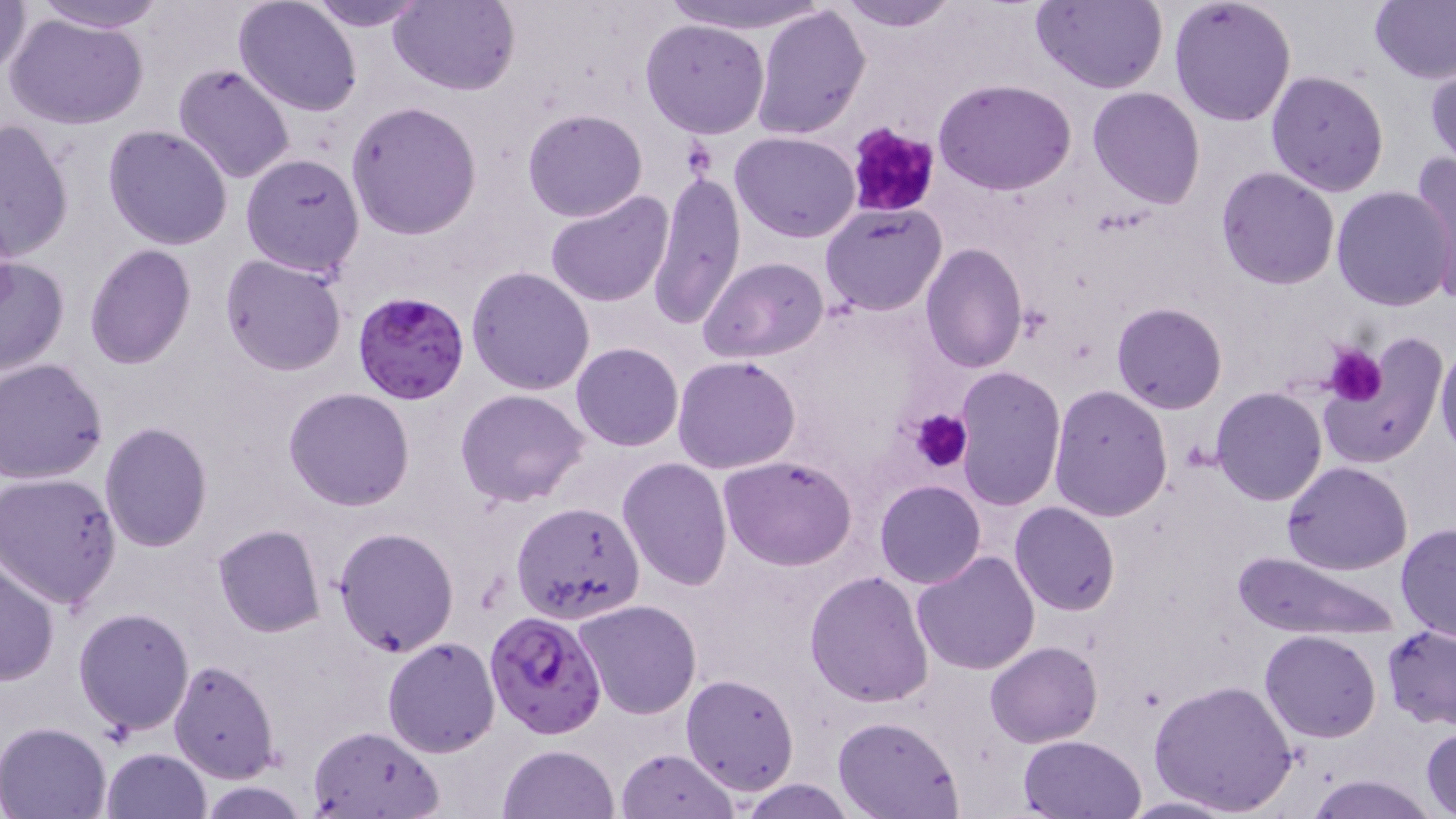
Plasmodium falciparum-infected red blood cell locations = approximate bounding boxes as (x1, y1, x2, y2) in pixels: (353, 291, 468, 405), (483, 608, 608, 740)
slide-level diagnosis = Plasmodium falciparum
uninfected red blood cell locations = approximate bounding boxes as (x1, y1, x2, y2) in pixels: (0, 0, 34, 82), (28, 0, 169, 33), (306, 0, 432, 30), (390, 0, 517, 96), (663, 0, 836, 36), (834, 0, 963, 31), (1030, 0, 1168, 92), (1168, 0, 1297, 126), (1368, 0, 1456, 84), (235, 1, 363, 117), (751, 4, 871, 139), (5, 12, 149, 131), (640, 18, 770, 138), (172, 63, 297, 185), (1426, 66, 1456, 168), (1266, 69, 1390, 197), (934, 78, 1077, 195), (1087, 85, 1207, 210), (346, 100, 482, 239), (521, 108, 649, 222), (0, 119, 72, 262), (103, 124, 233, 250), (731, 131, 860, 241), (1411, 151, 1456, 298), (240, 154, 365, 279), (1215, 165, 1341, 289), (646, 172, 747, 329), (1331, 186, 1454, 312), (544, 190, 675, 310), (819, 203, 948, 316), (920, 243, 1026, 371), (83, 244, 196, 369), (220, 253, 348, 375), (0, 255, 70, 379), (699, 257, 830, 364), (467, 265, 597, 394), (1111, 302, 1226, 414), (1322, 330, 1445, 468), (1435, 338, 1456, 464), (571, 343, 683, 451), (673, 356, 801, 474), (1, 358, 109, 484), (953, 364, 1066, 511), (1048, 384, 1174, 522), (1209, 387, 1328, 507), (283, 388, 414, 511), (456, 388, 588, 508), (99, 422, 212, 552), (720, 456, 857, 570), (617, 457, 734, 591), (1280, 462, 1414, 576), (0, 474, 122, 608), (875, 479, 986, 588), (1009, 502, 1120, 617), (511, 503, 642, 627), (1396, 522, 1455, 643), (213, 525, 325, 638), (333, 526, 459, 657), (1234, 550, 1399, 641), (911, 551, 1041, 676), (0, 557, 59, 687), (804, 570, 933, 707), (574, 600, 703, 720), (73, 607, 195, 737), (1382, 625, 1456, 729), (1260, 630, 1382, 743), (382, 636, 501, 757), (985, 641, 1102, 748), (168, 660, 278, 782), (680, 673, 799, 795), (1150, 677, 1297, 817), (832, 715, 963, 818), (0, 722, 114, 818), (306, 726, 445, 819), (1421, 728, 1455, 817), (1018, 735, 1147, 819), (499, 744, 619, 819), (100, 748, 212, 819), (615, 748, 739, 819), (1304, 775, 1438, 818), (736, 777, 856, 818), (1116, 795, 1242, 818)
preparation = thin blood film
image size = 1456×819 pixels
field of view = one of a larger specimen
platelet locations = approximate bounding boxes as (x1, y1, x2, y2) in pixels: (843, 121, 943, 220), (1322, 345, 1387, 404), (910, 410, 971, 473)
magnification = 1000x
stain = May-Grünwald-Giemsa
modality = light microscopy